Locate every Plasmodium vivax-infected red blood cell.
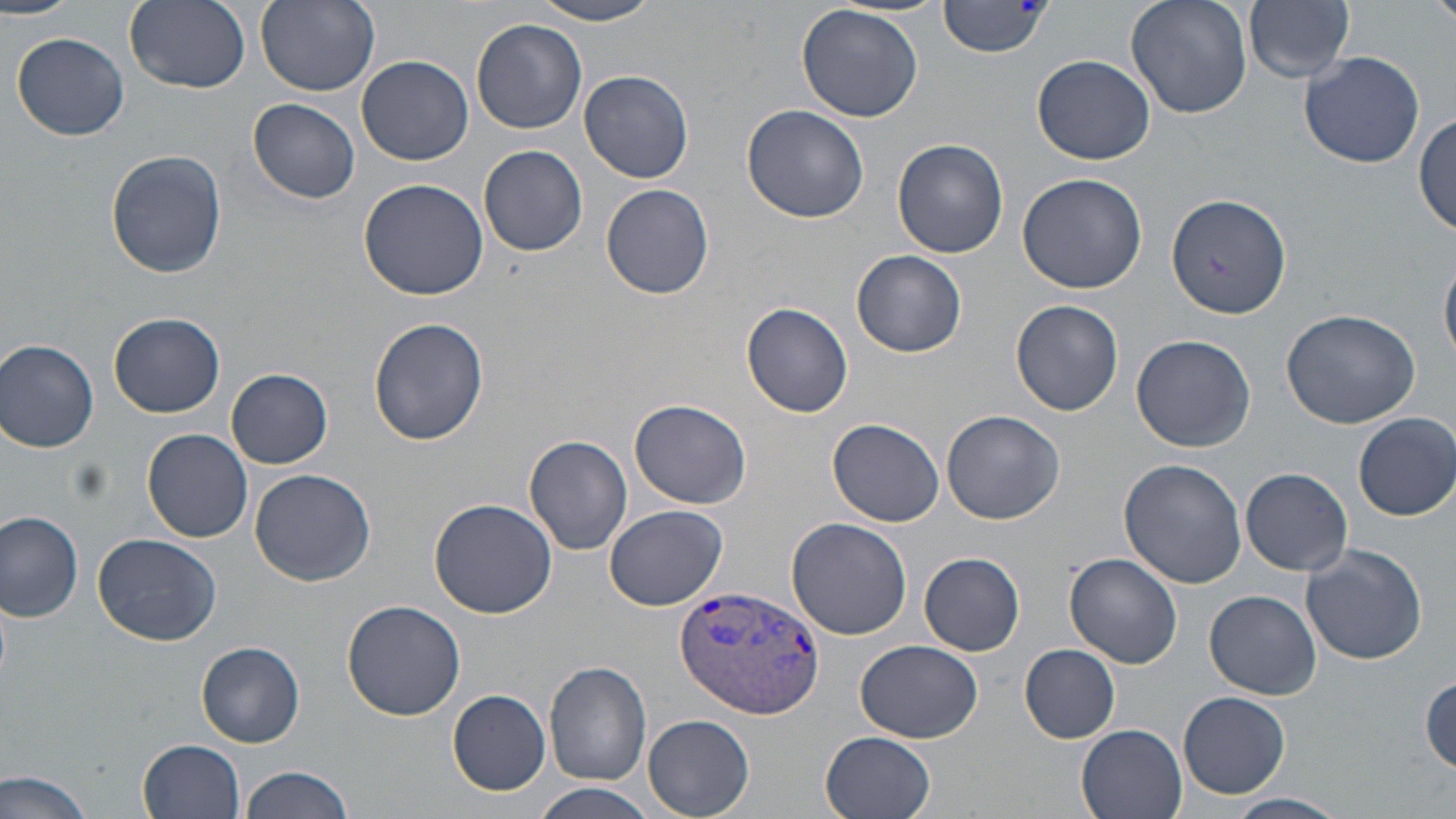
Approximate bounding boxes as named x1/y1/x2/y2 corners in pixels.
Plasmodium vivax-infected red blood cells: (x1=676, y1=583, x2=827, y2=718).

slide-level diagnosis = Plasmodium vivax
image size = 1456×819 pixels
field of view = single
uninfected red blood cell locations = approximate bounding boxes as named x1/y1/x2/y2 corners in pixels: (x1=0, y1=0, x2=82, y2=19), (x1=124, y1=0, x2=251, y2=93), (x1=254, y1=0, x2=379, y2=94), (x1=939, y1=0, x2=1052, y2=58), (x1=1128, y1=0, x2=1253, y2=119), (x1=530, y1=1, x2=666, y2=26), (x1=1244, y1=1, x2=1356, y2=84), (x1=797, y1=4, x2=924, y2=123), (x1=472, y1=17, x2=589, y2=134), (x1=12, y1=31, x2=130, y2=141), (x1=1297, y1=49, x2=1424, y2=169), (x1=356, y1=55, x2=473, y2=166), (x1=1032, y1=55, x2=1156, y2=166), (x1=579, y1=69, x2=695, y2=182), (x1=246, y1=98, x2=362, y2=204), (x1=741, y1=104, x2=870, y2=223), (x1=1413, y1=113, x2=1455, y2=237), (x1=893, y1=137, x2=1008, y2=258), (x1=480, y1=145, x2=588, y2=257), (x1=106, y1=149, x2=227, y2=279), (x1=1017, y1=173, x2=1148, y2=294), (x1=359, y1=178, x2=488, y2=301), (x1=601, y1=182, x2=715, y2=300), (x1=1166, y1=189, x2=1292, y2=318), (x1=853, y1=250, x2=967, y2=357), (x1=1441, y1=257, x2=1456, y2=364), (x1=1011, y1=301, x2=1123, y2=416), (x1=742, y1=302, x2=853, y2=419), (x1=1281, y1=309, x2=1420, y2=428), (x1=109, y1=312, x2=225, y2=417), (x1=369, y1=318, x2=487, y2=444), (x1=1131, y1=335, x2=1257, y2=454), (x1=0, y1=339, x2=99, y2=452), (x1=227, y1=368, x2=333, y2=468), (x1=630, y1=398, x2=752, y2=509), (x1=941, y1=409, x2=1065, y2=524), (x1=1353, y1=412, x2=1456, y2=520), (x1=828, y1=417, x2=945, y2=526), (x1=144, y1=429, x2=254, y2=542), (x1=524, y1=435, x2=633, y2=555), (x1=1119, y1=459, x2=1246, y2=588), (x1=1241, y1=467, x2=1353, y2=576), (x1=249, y1=468, x2=376, y2=586), (x1=430, y1=498, x2=556, y2=618), (x1=603, y1=504, x2=729, y2=611), (x1=0, y1=511, x2=84, y2=621), (x1=786, y1=517, x2=914, y2=640), (x1=91, y1=532, x2=221, y2=645), (x1=1301, y1=542, x2=1428, y2=666), (x1=919, y1=551, x2=1025, y2=656), (x1=1065, y1=553, x2=1183, y2=668), (x1=1205, y1=588, x2=1321, y2=698), (x1=342, y1=601, x2=466, y2=720), (x1=857, y1=640, x2=983, y2=742), (x1=197, y1=641, x2=306, y2=747), (x1=1019, y1=644, x2=1121, y2=743), (x1=545, y1=661, x2=652, y2=786), (x1=1421, y1=674, x2=1456, y2=775), (x1=447, y1=688, x2=552, y2=796), (x1=1178, y1=690, x2=1290, y2=799), (x1=642, y1=714, x2=755, y2=818), (x1=1076, y1=722, x2=1190, y2=819), (x1=820, y1=732, x2=936, y2=819), (x1=137, y1=738, x2=243, y2=817), (x1=239, y1=765, x2=357, y2=819), (x1=1, y1=767, x2=99, y2=819), (x1=533, y1=784, x2=658, y2=819), (x1=1227, y1=793, x2=1347, y2=819)
stain = May-Grünwald-Giemsa
modality = light microscopy
preparation = thin blood film
magnification = 1000x